Classify this cell by malaria status.
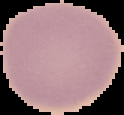
Uninfected.

Image is 124×115 pixels. From a thin blood film. Cell region segmented out of the field of view; the surrounding area is masked to black.